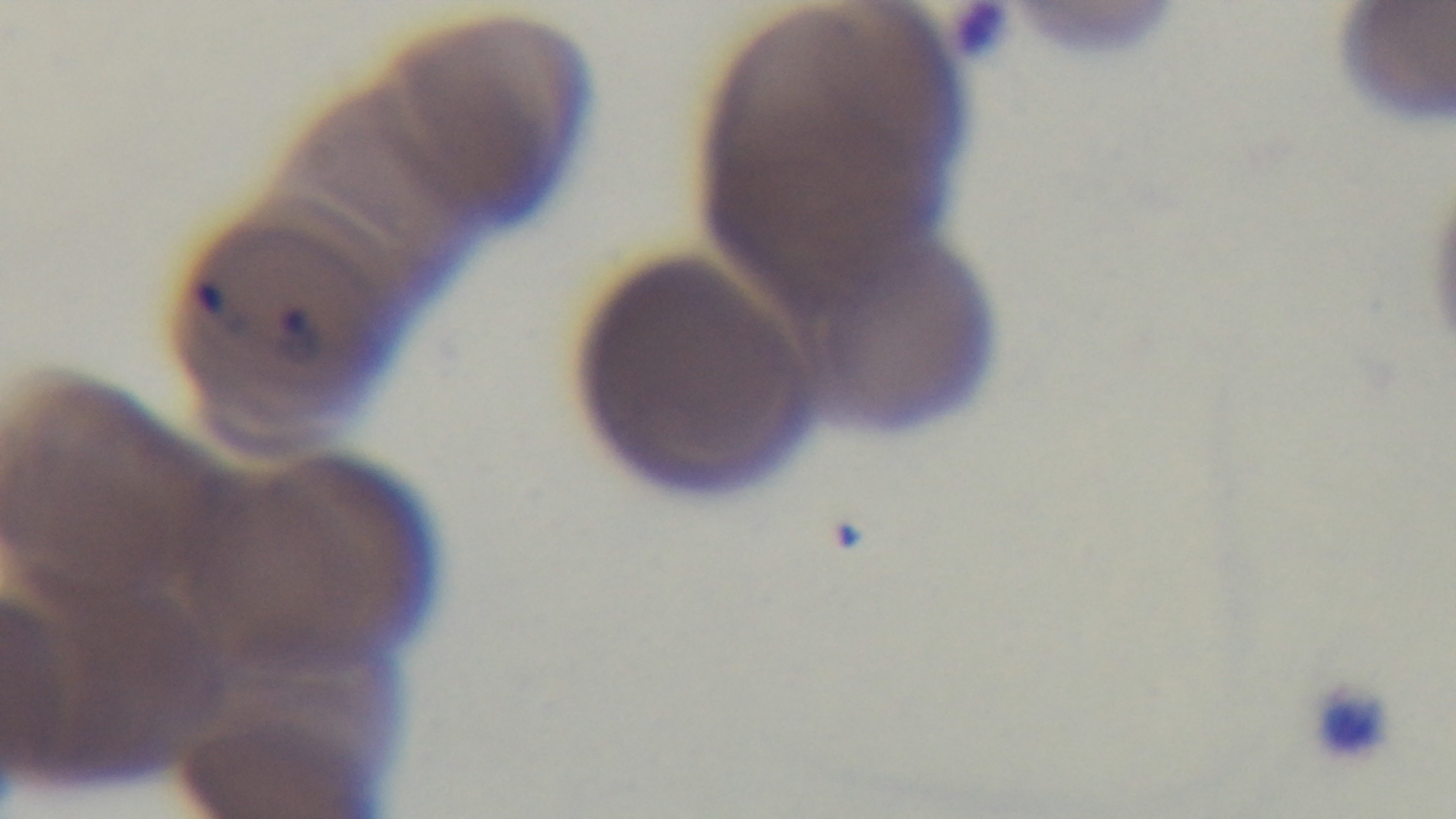

malaria status = infected
modality = light microscopy
stain = Giemsa
capture = mounted 4K digital camera
preparation = thin
objective = 100x oil immersion
field of view = one from the slide